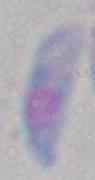

modality = photomicrograph
magnification = 1000x
identification = Toxoplasma gondii